Assess the morphology of the erythrocytes.
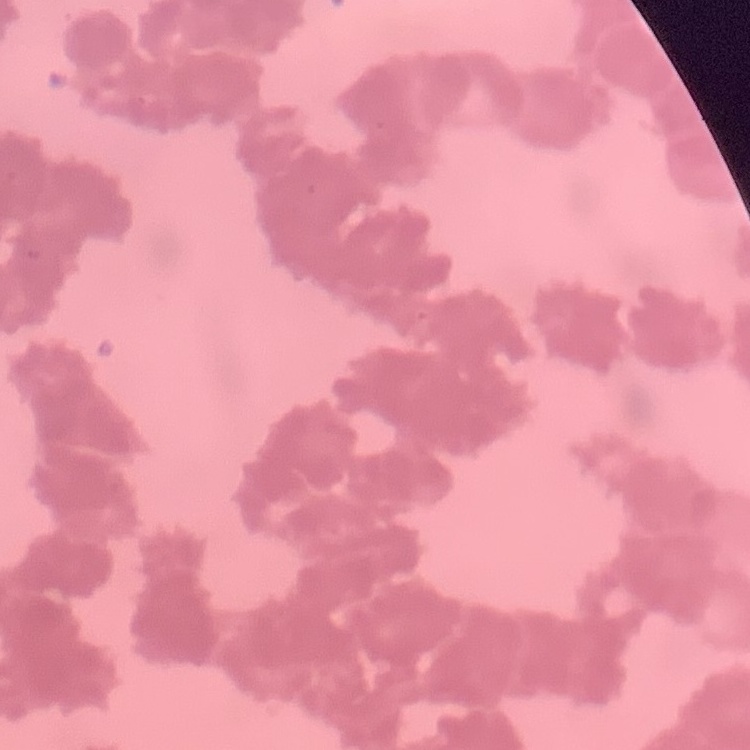
They show rouleaux formation.

Summary:
  - Preparation: thin peripheral smear
  - Stain: Field's or Giemsa
  - Image type: square crop of a larger photomicrograph